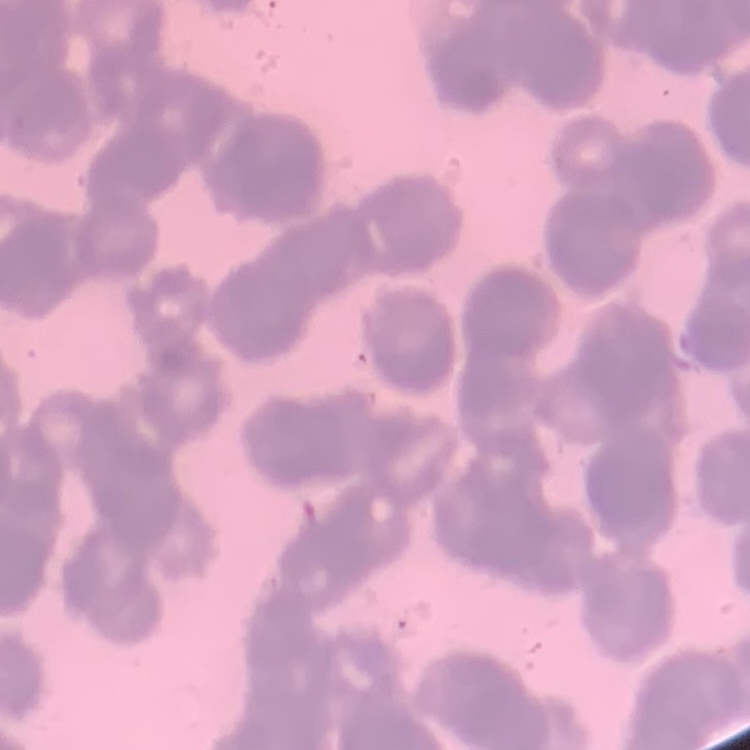

Summary:
  - Red blood cell morphology: rouleaux formation
  - Image type: square crop of a larger photomicrograph
  - Preparation: thin peripheral smear
  - Stain: Field's or Giemsa